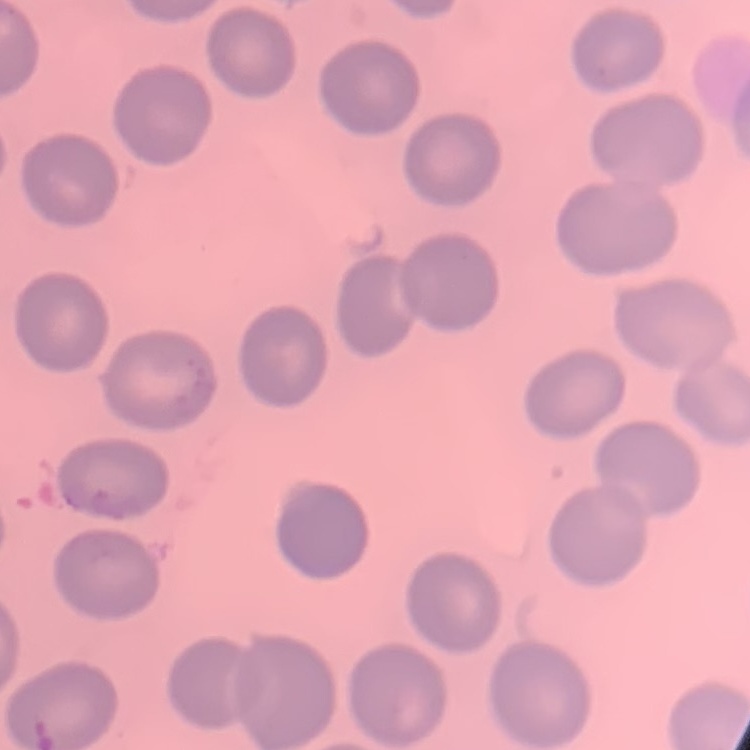 The red blood cells exhibit no rouleaux formation. One tile cut from a larger photomicrograph. Field's or Giemsa stain. Thin peripheral smear.